Point out each Plasmodium parasite.
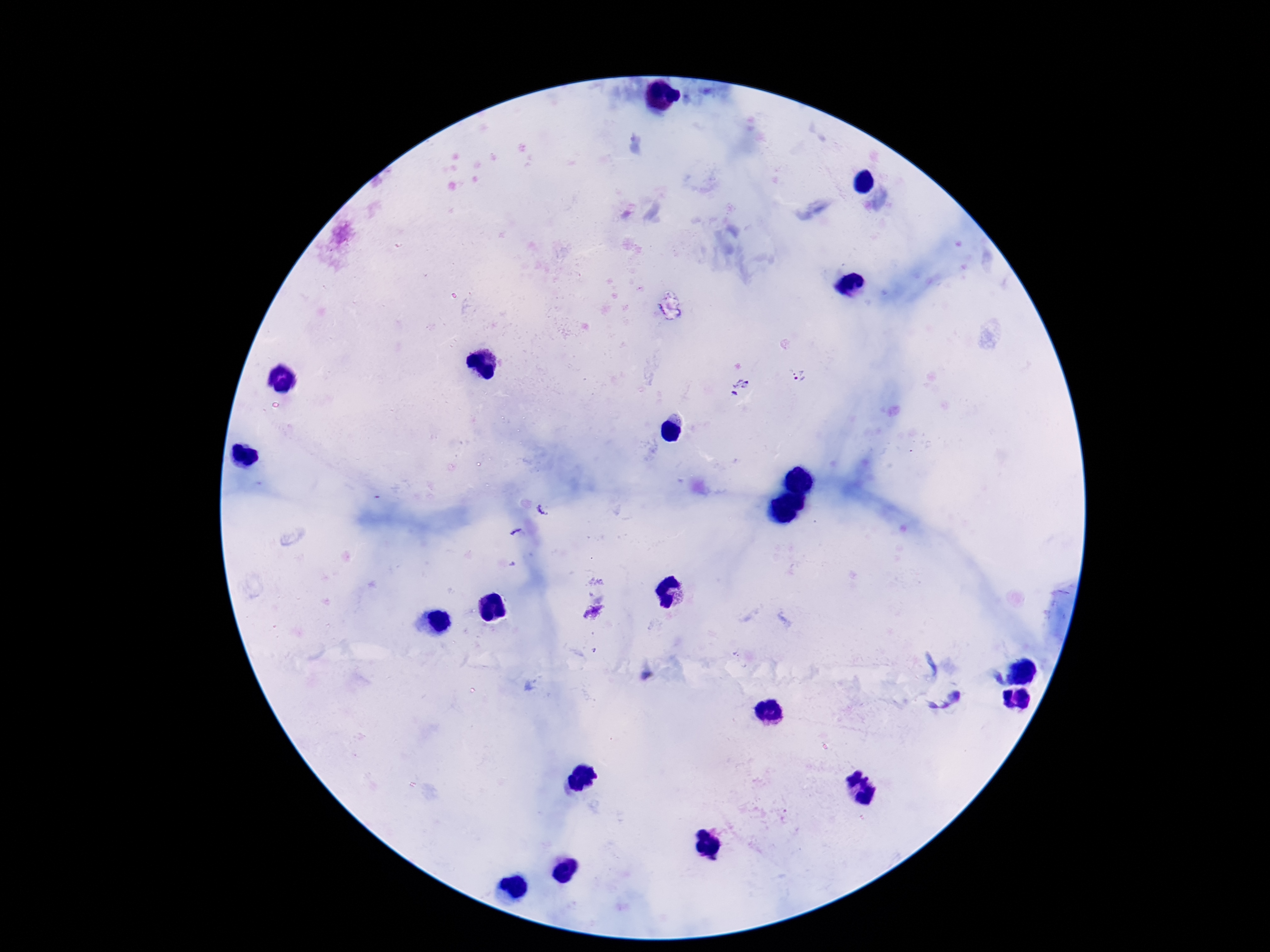
Approximate centers as [x, y] in pixels.
Plasmodium parasites: [798, 373], [738, 389].

{
  "patient_malaria_status": "positive",
  "field_of_view": "one from this slide",
  "magnification": "100x",
  "preparation": "thick blood film",
  "capture": "smartphone camera through the microscope eyepiece",
  "stain": "Giemsa",
  "image_size": "1270×952 pixels"
}